Classify this cell by malaria status.
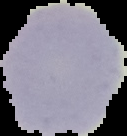

It is uninfected.

{
  "preparation": "thin blood smear",
  "image_type": "cell region segmented out of the field of view; surrounding area masked to black",
  "image_size": "127×136 pixels"
}